Locate every Plasmodium parasite.
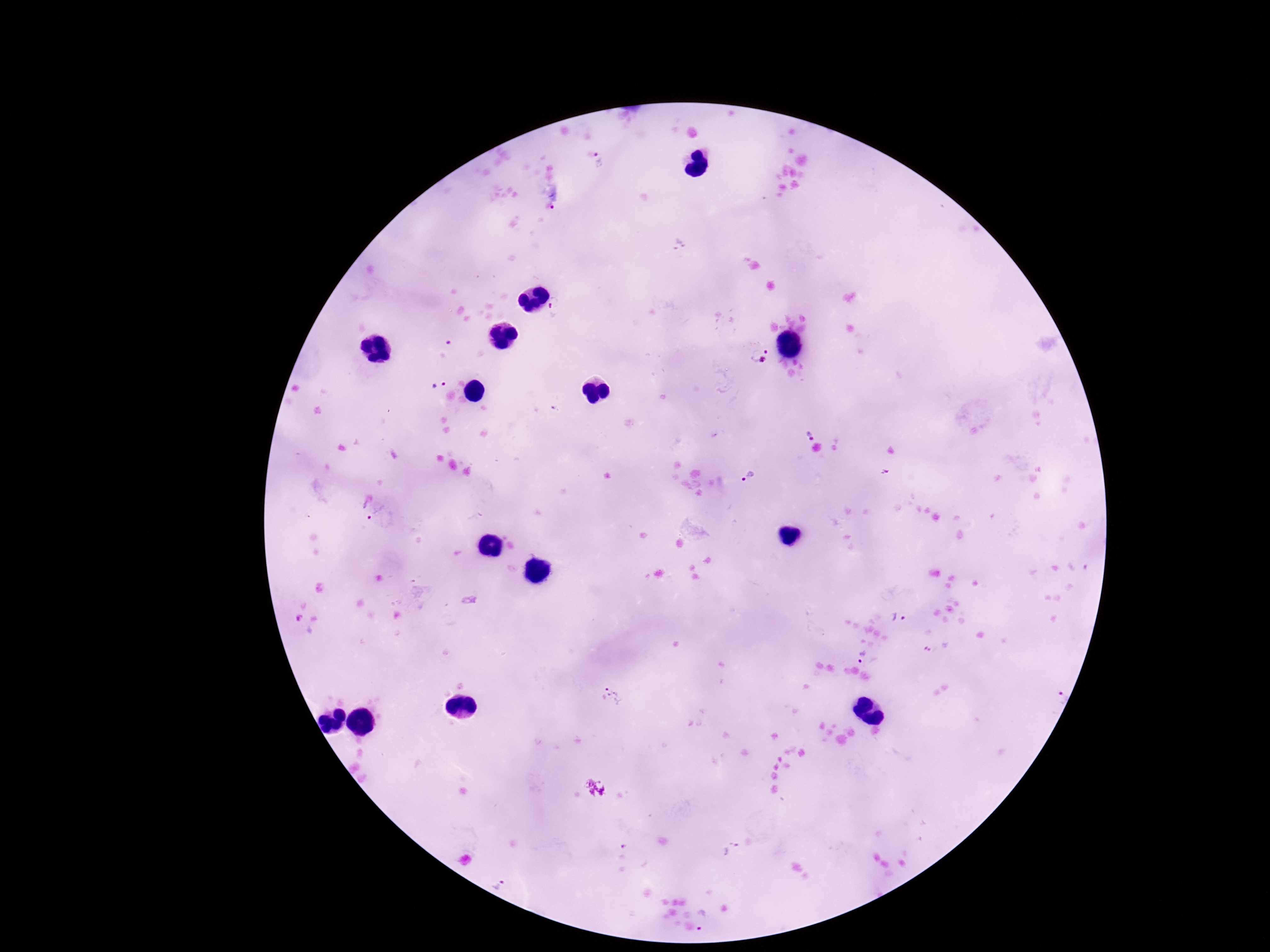

Approximate object centers, in pixels from the top-left corner.
Plasmodium parasites: (x=600, y=161), (x=556, y=199), (x=758, y=355), (x=437, y=384), (x=811, y=429), (x=746, y=476), (x=368, y=510), (x=899, y=616), (x=861, y=657), (x=609, y=698), (x=504, y=885), (x=702, y=920).

image_size: 1270×952 pixels
patient_malaria_status: infected
stain: Giemsa
field_of_view: single
magnification: 100x
capture: smartphone camera through the microscope eyepiece
preparation: thick blood film